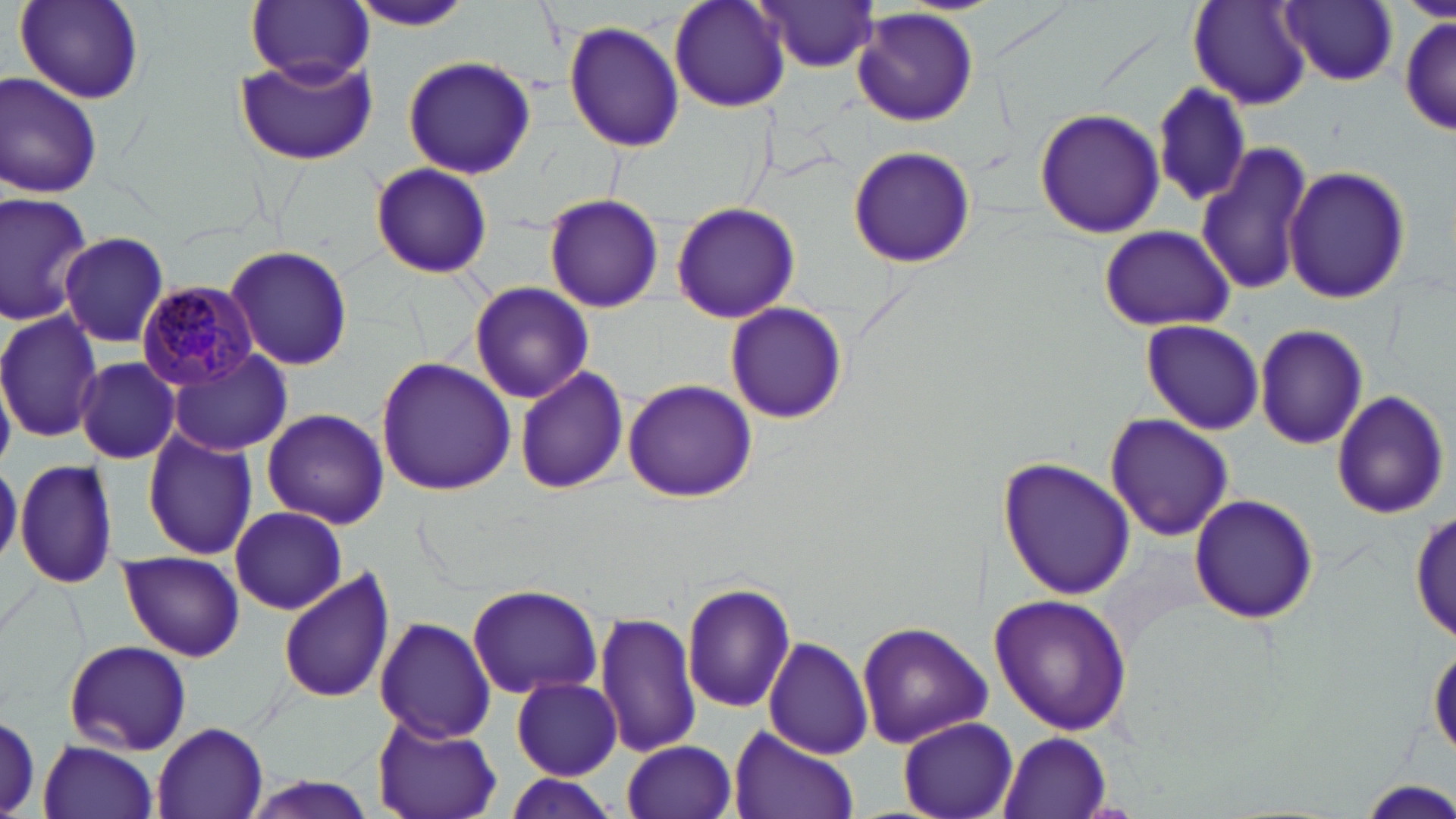
slide_level_diagnosis: Plasmodium malariae
stain: May-Grünwald-Giemsa
magnification: 1000x
preparation: thin blood smear
image_size: 1456×819 pixels
modality: optical microscopy
plasmodium_malariae_infected_red_blood_cell_locations: 'approximate bounding boxes as [x1, y1, x2, y2] in pixels: [137, 282, 261, 391]'
uninfected_red_blood_cell_locations: 'approximate bounding boxes as [x1, y1, x2, y2] in pixels: [248, 0, 373, 85], [346, 0, 477, 31], [667, 0, 791, 114], [14, 1, 145, 105], [752, 1, 883, 72], [1278, 1, 1397, 86], [1189, 2, 1309, 109], [852, 9, 980, 127], [1399, 15, 1455, 137], [563, 21, 684, 152], [234, 55, 376, 167], [401, 55, 537, 179], [0, 72, 103, 201], [1150, 81, 1251, 208], [1033, 108, 1165, 239], [1195, 139, 1313, 296], [846, 144, 976, 268], [369, 163, 495, 279], [1284, 164, 1412, 304], [0, 190, 93, 325], [543, 193, 666, 313], [670, 202, 802, 323], [1098, 224, 1237, 332], [59, 231, 170, 349], [224, 245, 354, 372], [470, 282, 594, 402], [724, 302, 848, 425], [1, 309, 102, 443], [1140, 320, 1266, 436], [1255, 321, 1369, 449], [167, 347, 292, 454], [376, 356, 517, 494], [75, 357, 180, 462], [514, 366, 628, 496], [621, 377, 757, 502], [1330, 390, 1449, 519], [262, 407, 391, 531], [1105, 413, 1235, 541], [141, 427, 258, 559], [998, 458, 1136, 599], [0, 459, 21, 567], [14, 459, 120, 590], [1189, 494, 1318, 624], [231, 507, 348, 615], [1410, 511, 1454, 642], [118, 551, 244, 662], [278, 567, 393, 705], [466, 583, 603, 700], [680, 584, 795, 716], [991, 593, 1134, 735], [595, 610, 700, 758], [375, 616, 496, 742], [856, 621, 991, 749], [763, 637, 873, 759], [63, 640, 191, 755], [1428, 644, 1455, 763], [512, 677, 622, 779], [897, 715, 1018, 819], [372, 717, 502, 819], [152, 721, 270, 818], [727, 724, 861, 819], [999, 732, 1112, 819], [39, 739, 161, 819], [622, 740, 738, 818], [497, 774, 626, 819], [240, 775, 383, 819], [1363, 779, 1455, 815]'
field_of_view: one of a larger specimen